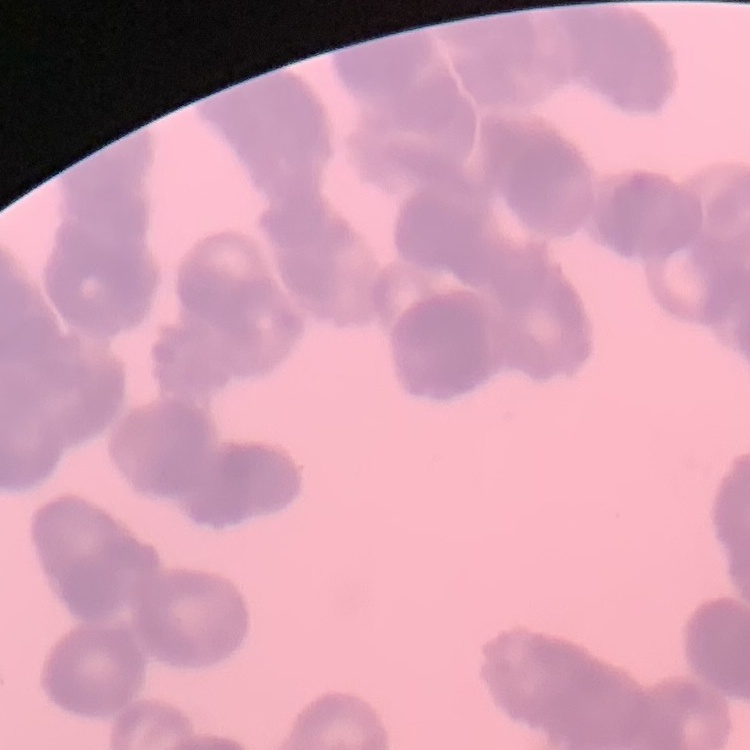

erythrocyte_morphology: rouleaux formation
image_type: one tile cut from a larger photomicrograph
stain: Field's or Giemsa
preparation: thin blood film